Assess this cell for malaria.
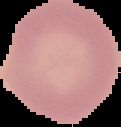

It is uninfected.

Image is 121×127 pixels. From a thin blood film. The area outside the segmented cell region is set to black.